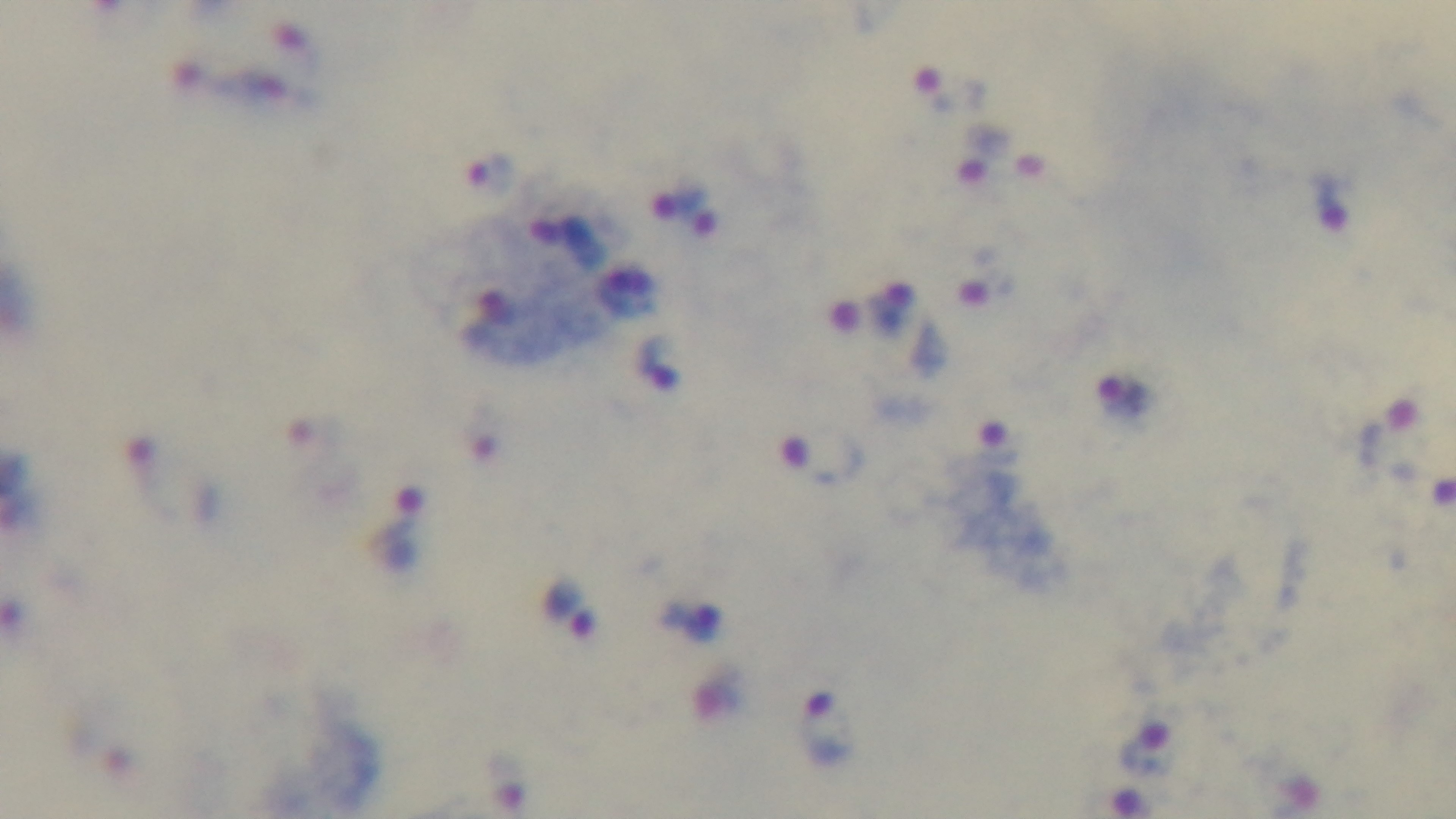
Summary:
  - Malaria status: infected
  - Modality: light microscopy
  - Capture: mounted 4K digital camera
  - Objective: 100x oil immersion
  - Preparation: thick
  - Stain: Giemsa
  - Field of view: one from the slide